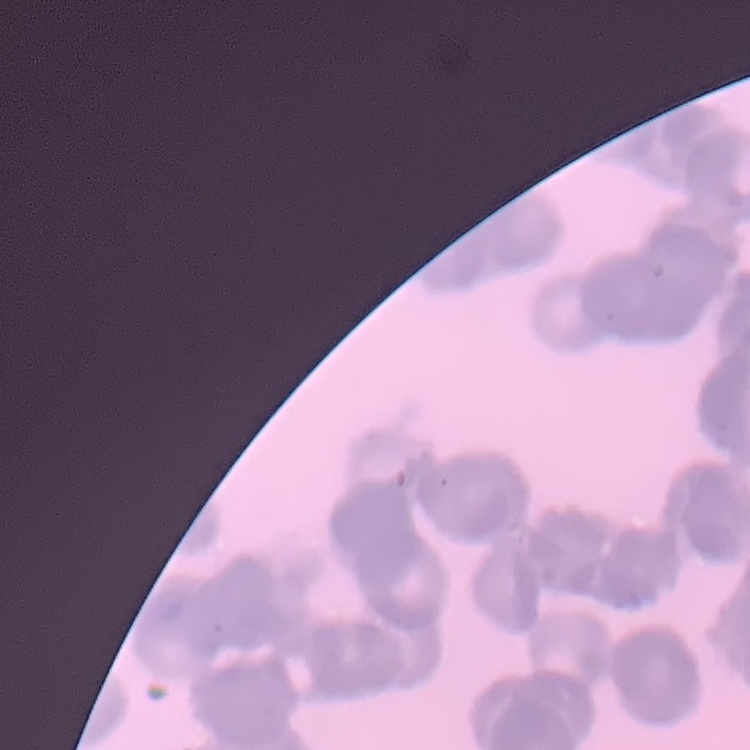

The red blood cells show rouleaux formation. Stained with either Field's or Giemsa. Square crop of a larger photomicrograph. Thin blood film.